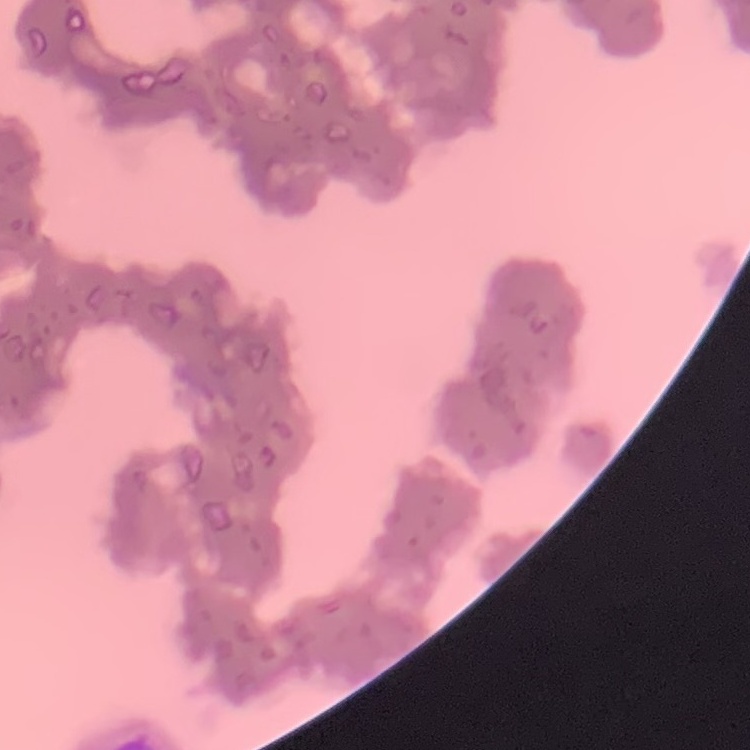 The red blood cells exhibit rouleaux formation. Thin blood film. Field's or Giemsa stain. One tile cut from a larger photomicrograph.